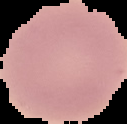

Summary:
  - Image size: 127×124 pixels
  - Image type: cell region segmented out of the field of view; surrounding area masked to black
  - Malaria status: uninfected
  - Preparation: thin blood smear